Identify the parasite.
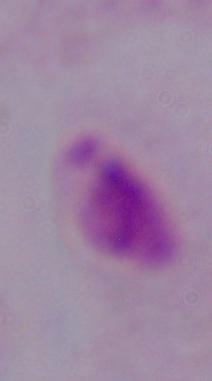

A trichomonad.

{
  "magnification": "1000x",
  "modality": "micrograph"
}